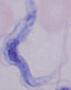
modality = photomicrograph
identification = trypanosome
magnification = 1000x